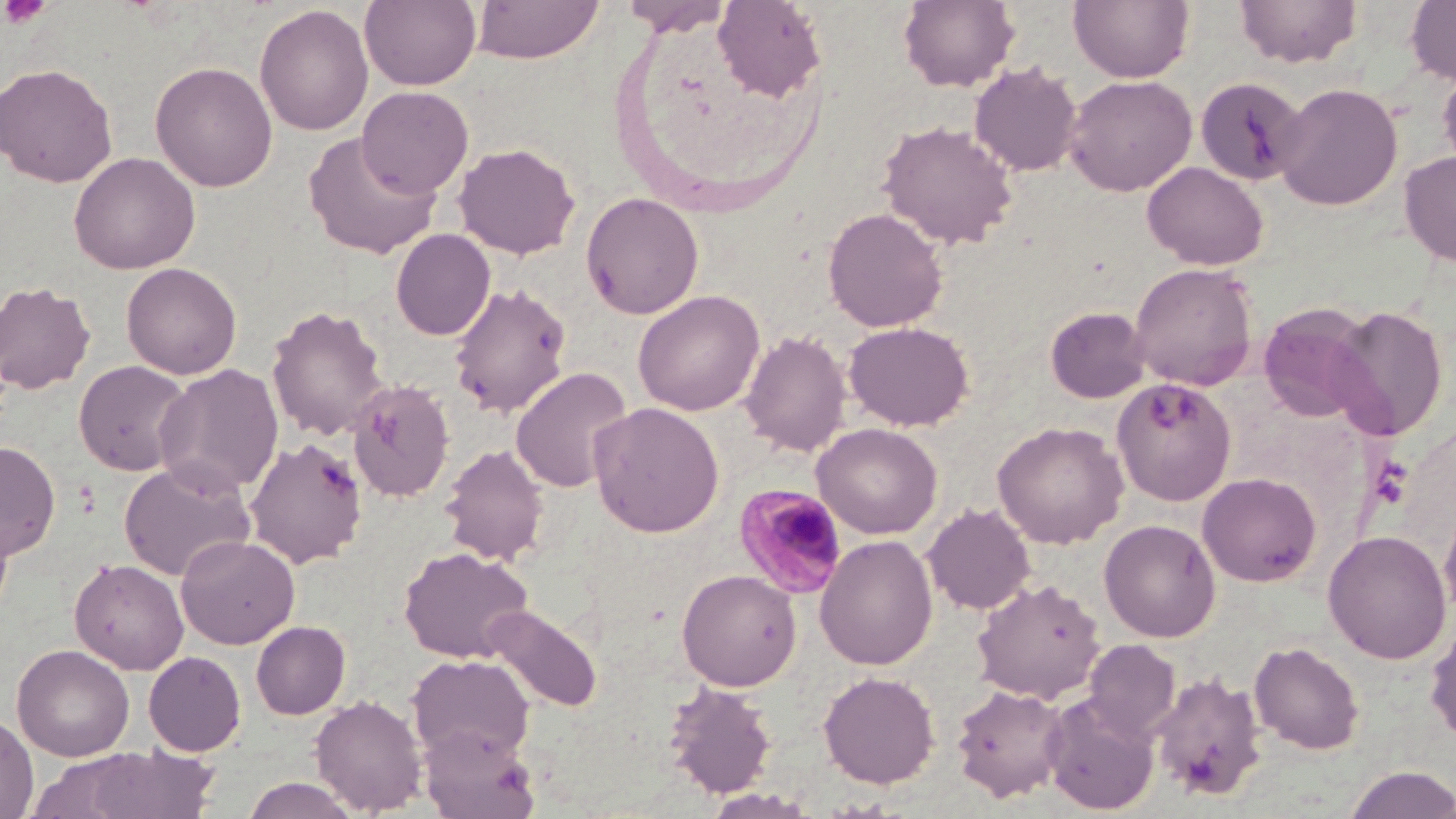

Approximate bounding boxes as (x1,y1)-(x2,y2) corner pairs in pixels. Plasmodium malariae-infected red blood cell locations: (734,483)-(849,599). Platelet locations: (1,0)-(52,30). Uninfected red blood cell locations: (360,0)-(481,90), (471,0)-(604,63), (620,0)-(730,35), (713,0)-(827,101), (898,0)-(1020,92), (1069,0)-(1195,83), (1405,0)-(1456,86), (1234,1)-(1362,69), (254,4)-(374,136), (150,60)-(278,192), (0,62)-(118,187), (969,62)-(1083,177), (1437,63)-(1456,179), (1065,74)-(1197,196), (1194,76)-(1308,186), (1273,82)-(1403,210), (357,86)-(474,197), (878,120)-(1018,249), (303,131)-(442,259), (454,142)-(580,259), (69,151)-(201,274), (1398,151)-(1456,267), (1141,161)-(1269,270), (581,191)-(704,320), (823,207)-(948,333), (390,229)-(495,340), (121,262)-(242,379), (1129,262)-(1259,390), (0,280)-(97,394), (448,281)-(573,418), (632,290)-(765,416), (1258,302)-(1377,423), (266,303)-(390,442), (1327,304)-(1450,440), (1044,306)-(1151,404), (843,321)-(974,431), (740,330)-(852,457), (73,360)-(194,476), (154,364)-(284,497), (511,366)-(633,492), (1110,377)-(1236,505), (347,379)-(455,503), (588,401)-(724,537), (992,421)-(1129,549), (812,422)-(942,538), (244,436)-(367,568), (0,442)-(60,560), (440,443)-(550,566), (118,458)-(256,582), (1198,472)-(1321,586), (1439,497)-(1456,622), (922,503)-(1035,615), (1099,518)-(1221,642), (1323,530)-(1452,664), (176,535)-(299,648), (814,535)-(938,670), (398,545)-(533,662), (69,558)-(189,674), (677,569)-(802,690), (973,578)-(1104,703), (481,604)-(602,713), (1425,617)-(1456,748), (251,620)-(350,719), (1084,640)-(1180,741), (1250,640)-(1363,755), (12,644)-(135,761), (143,651)-(246,756), (407,654)-(535,764), (1150,670)-(1268,803), (818,671)-(940,788), (664,681)-(777,798), (951,683)-(1070,802), (310,693)-(428,815), (1042,693)-(1161,815), (0,711)-(38,819), (420,725)-(540,819), (77,743)-(223,818), (1342,765)-(1456,819), (239,776)-(362,818), (702,788)-(821,819). Slide-level diagnosis: Plasmodium malariae. 1000x magnification. Optical microscopy. Image is 1456×819 pixels. One field of a larger specimen. Thin blood smear. May-Grünwald-Giemsa stain.